Name the parasite shown.
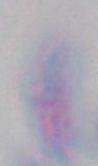
This is Toxoplasma gondii.

modality = micrograph
magnification = 1000x